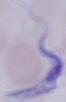
magnification = 1000x
modality = photomicrograph
identification = trypanosome